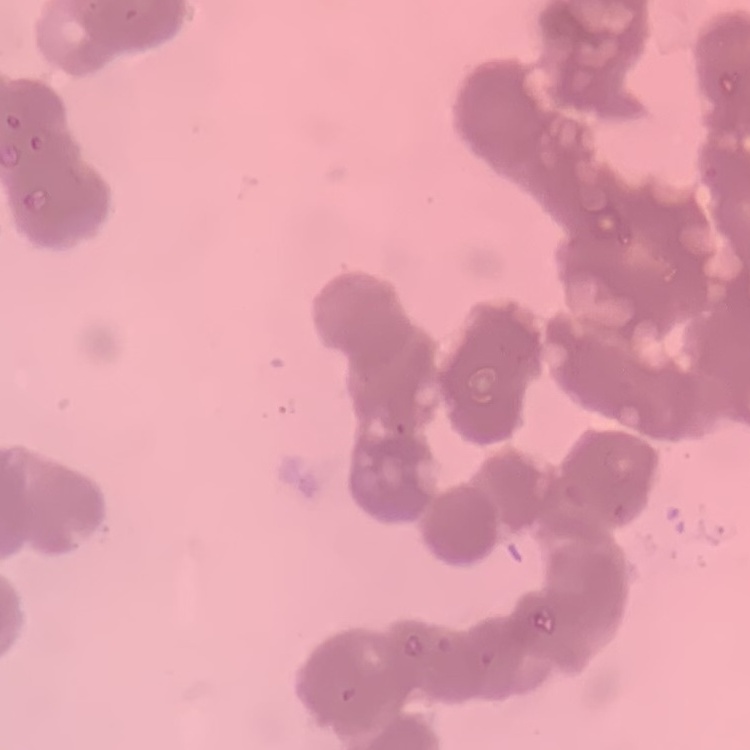
Summary:
  - Red blood cell morphology: rouleaux formation
  - Preparation: thin blood smear
  - Stain: Field's or Giemsa
  - Image type: square crop of a larger photomicrograph